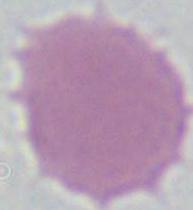

Captured at 1000x magnification. An erythrocyte is seen. Micrograph.